Classify this cell by malaria status.
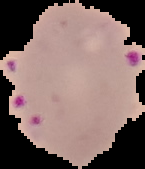
It is parasitized.

preparation = thin blood smear
image size = 145×169 pixels
image type = cell region segmented out of the field of view; surrounding area masked to black